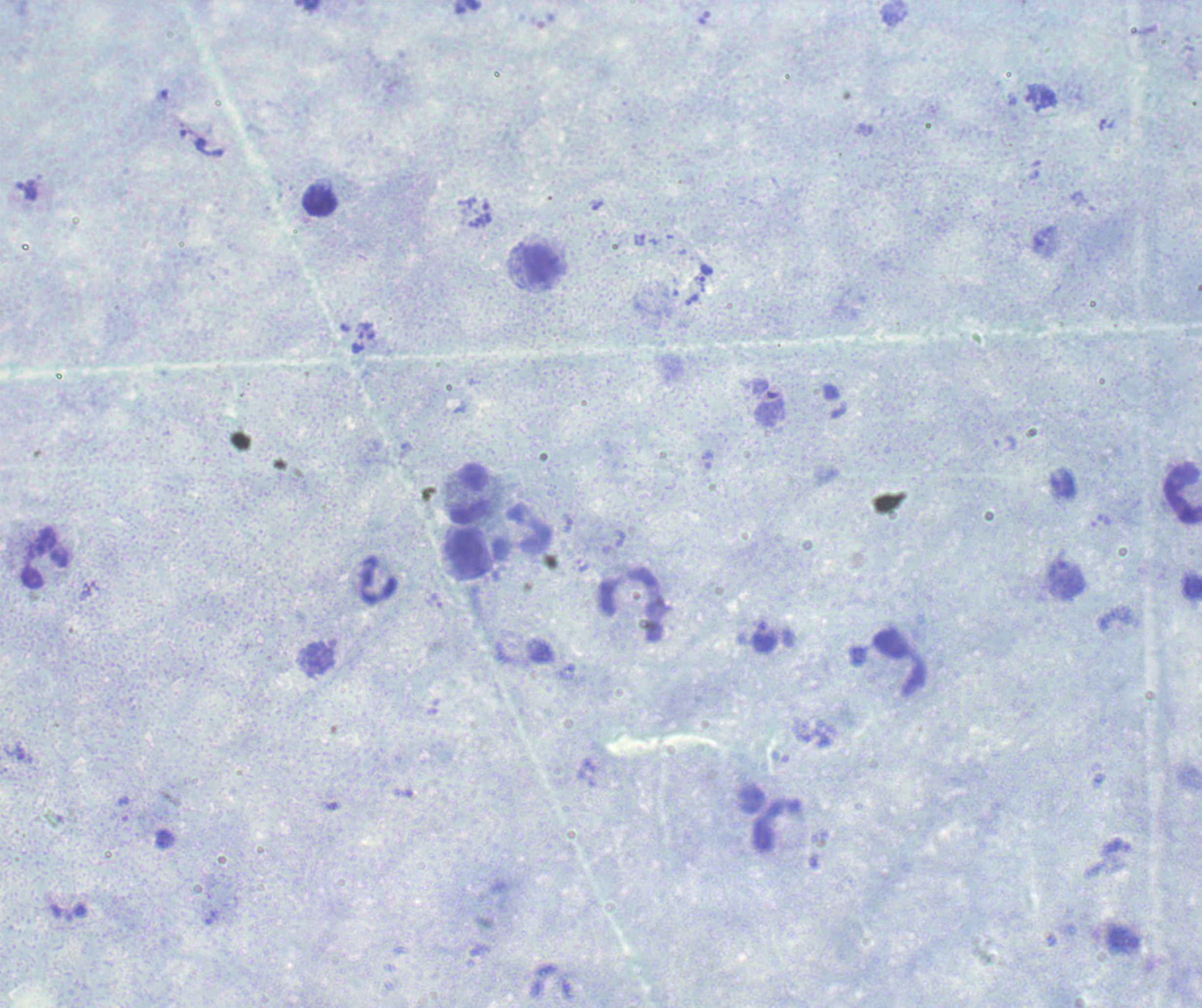
Romanowsky stain. One field from this slide. Thick smear of blood. Image is 1202×1008 pixels.